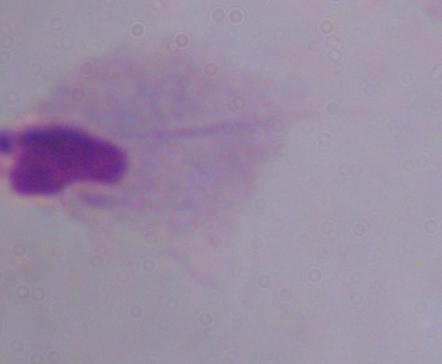

Summary:
  - Identification: trichomonad
  - Modality: photomicrograph
  - Magnification: 1000x